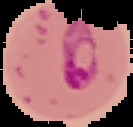

Image is 133×127 pixels. From a thin blood film. Result: Plasmodium parasites identified. Segmented cell region on a black background.